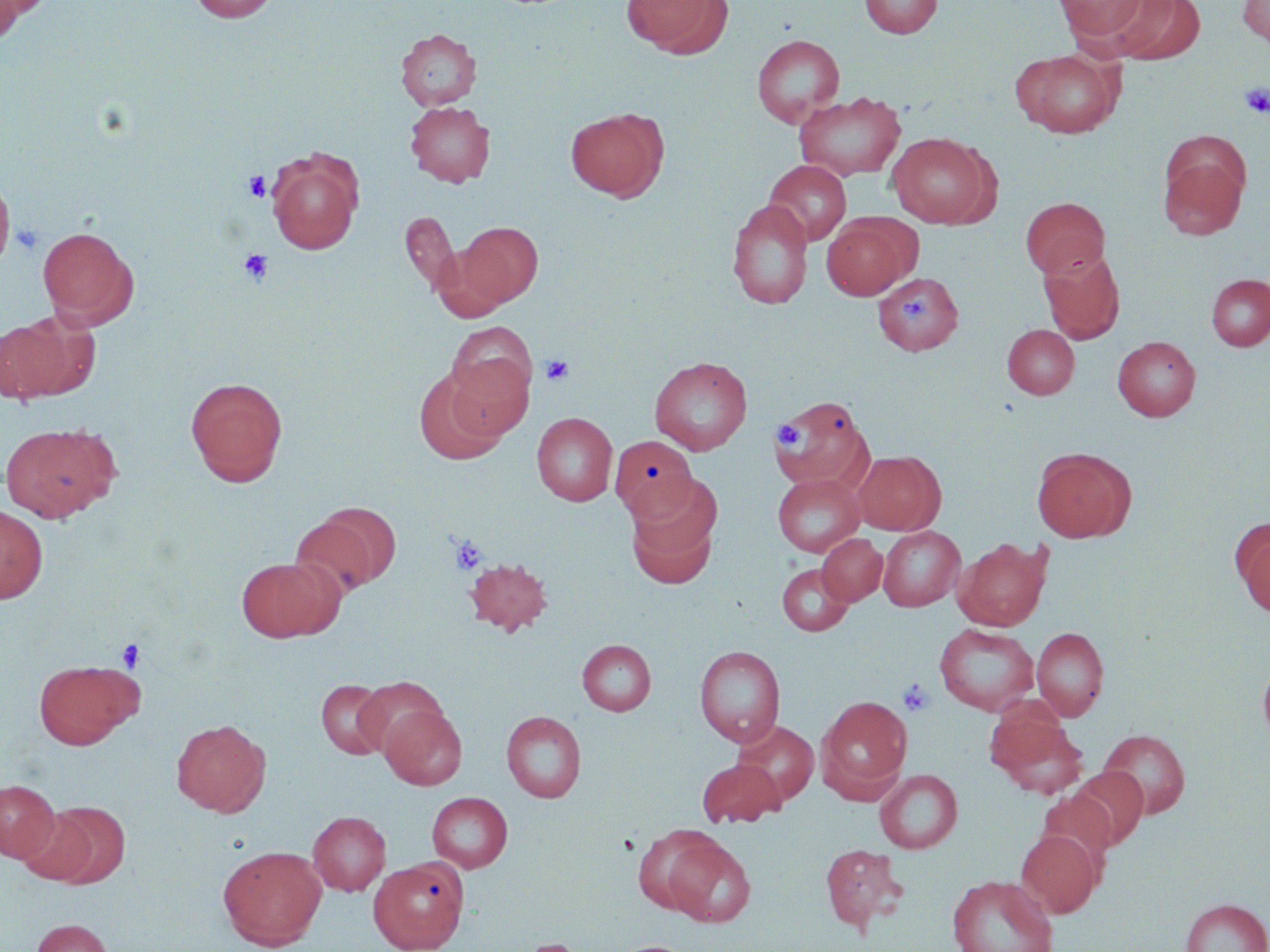

slide-level diagnosis = negative for blood parasites
modality = optical microscopy
stain = May-Grünwald-Giemsa
image size = 1270×952 pixels
field of view = one of a larger specimen
preparation = thin blood film
uninfected red blood cell locations = approximate bounding boxes as (x1,y1)-(x2,y2) corner pairs in pixels: (0,0)-(27,44), (188,0)-(280,22), (620,0)-(728,56), (859,0)-(941,39), (1053,0)-(1153,45), (1110,0)-(1204,65), (1237,0)-(1270,50), (396,28)-(481,110), (751,34)-(845,128), (1010,48)-(1124,138), (794,90)-(907,181), (404,102)-(495,187), (565,107)-(669,202), (887,132)-(997,228), (1158,142)-(1250,241), (267,152)-(361,254), (764,159)-(852,245), (0,173)-(16,272), (1021,197)-(1109,278), (726,199)-(813,309), (401,212)-(460,294), (821,214)-(919,299), (456,221)-(544,307), (37,225)-(138,327), (1039,248)-(1126,344), (873,272)-(964,356), (1206,274)-(1270,351), (1,311)-(95,402), (446,322)-(538,415), (1003,324)-(1080,399), (1113,336)-(1200,421), (649,356)-(753,455), (414,366)-(511,465), (185,376)-(288,487), (771,395)-(873,490), (532,412)-(617,506), (1,422)-(119,522), (610,435)-(698,520), (1031,447)-(1135,543), (852,450)-(946,535), (772,473)-(866,557), (626,478)-(722,588), (0,505)-(49,603), (290,506)-(398,600), (1233,521)-(1270,619), (877,526)-(965,612), (817,534)-(887,606), (953,537)-(1053,630), (235,557)-(341,642), (465,557)-(553,636), (777,563)-(854,636), (934,623)-(1039,716), (1031,627)-(1109,720), (577,639)-(655,715), (694,645)-(785,747), (1257,654)-(1270,749), (33,658)-(143,750), (353,676)-(449,759), (316,679)-(395,760), (817,694)-(913,800), (379,705)-(467,790), (501,710)-(587,802), (989,711)-(1088,798), (171,719)-(271,816), (732,720)-(819,807), (1098,729)-(1191,819), (697,759)-(783,827), (1065,766)-(1148,850), (874,769)-(963,853), (0,779)-(59,861), (427,791)-(513,872), (15,806)-(103,886), (308,811)-(391,895), (633,827)-(726,914), (1015,829)-(1102,918), (662,836)-(756,927), (218,844)-(327,950), (820,844)-(909,933), (369,858)-(468,952), (947,874)-(1059,952), (1180,898)-(1269,952), (31,918)-(113,952), (515,938)-(595,952), (606,940)-(703,952)
platelet locations = approximate bounding boxes as (x1,y1)-(x2,y2) corner pairs in pixels: (1240,83)-(1270,118), (243,171)-(271,201), (9,220)-(45,255), (238,249)-(273,285), (902,295)-(931,324), (540,354)-(574,386), (771,420)-(805,450), (449,535)-(487,575), (116,638)-(145,672), (898,678)-(935,717)
magnification = 1000x